Name the parasite shown.
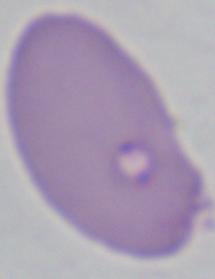
Babesia.

Summary:
  - Magnification: 1000x
  - Modality: photomicrograph